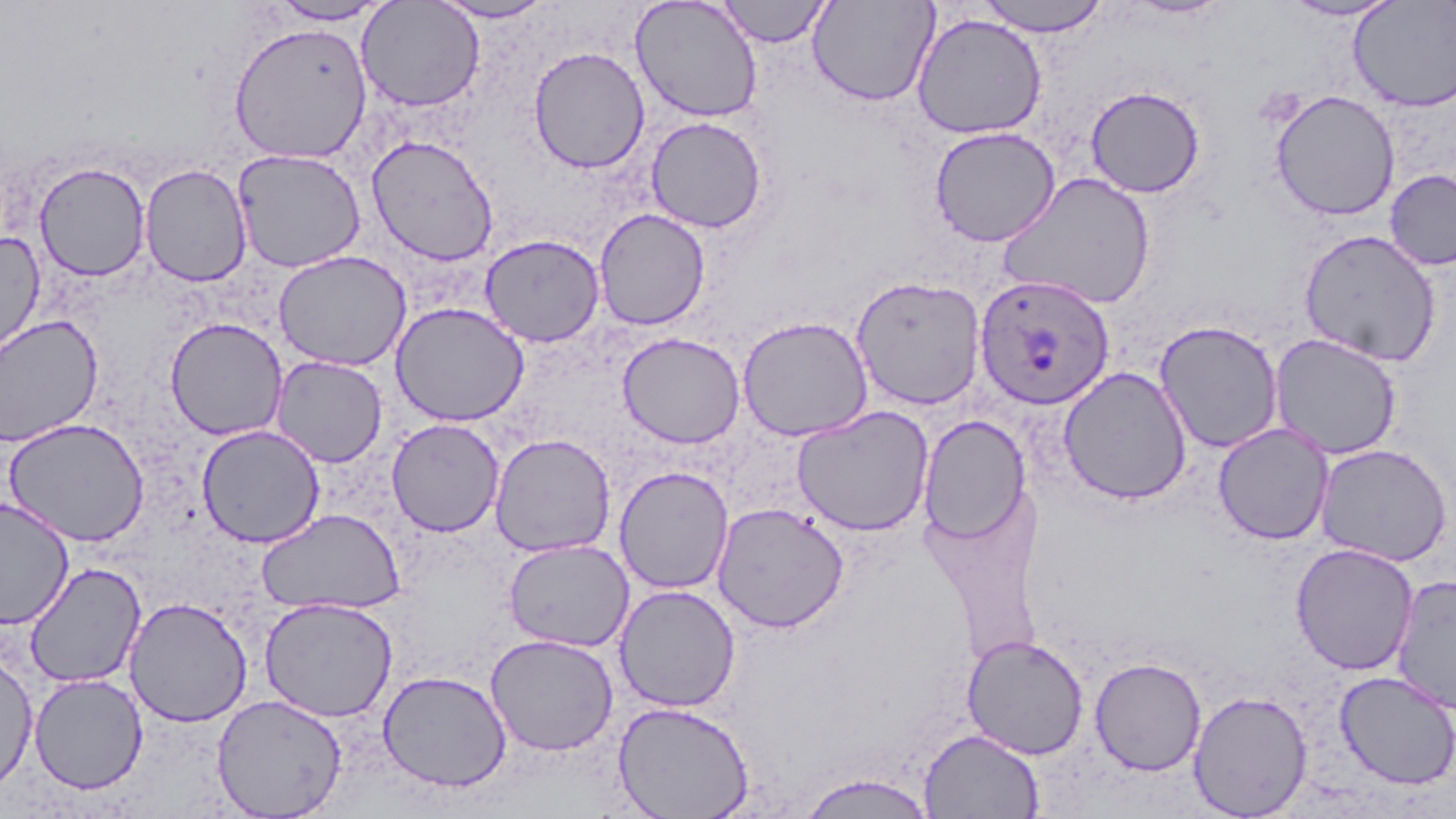 Approximate bounding boxes as (x1, y1, x2, y2) in pixels. Plasmodium ovale-infected red blood cell locations: (973, 275, 1114, 410). Uninfected red blood cell locations: (428, 0, 557, 23), (630, 0, 763, 123), (717, 0, 833, 47), (807, 0, 940, 107), (974, 0, 1111, 36), (1120, 0, 1234, 20), (1280, 0, 1403, 22), (269, 1, 392, 26), (356, 1, 485, 112), (1349, 1, 1456, 113), (911, 13, 1047, 139), (228, 21, 374, 164), (528, 46, 650, 174), (1084, 85, 1206, 198), (1270, 89, 1401, 221), (646, 116, 768, 233), (929, 126, 1060, 246), (366, 134, 499, 266), (232, 149, 366, 273), (34, 160, 150, 281), (139, 163, 253, 287), (1385, 168, 1456, 271), (997, 171, 1156, 310), (593, 208, 710, 331), (1298, 228, 1442, 366), (0, 231, 46, 363), (479, 234, 606, 347), (273, 250, 411, 371), (851, 275, 986, 411), (391, 302, 529, 427), (0, 314, 104, 447), (736, 315, 873, 441), (165, 317, 288, 441), (1154, 320, 1284, 454), (618, 332, 745, 449), (1269, 332, 1403, 460), (271, 356, 388, 468), (1057, 366, 1193, 505), (791, 405, 934, 537), (918, 416, 1031, 543), (3, 418, 151, 547), (386, 418, 505, 537), (1213, 423, 1333, 544), (196, 424, 326, 548), (489, 433, 616, 558), (1314, 443, 1453, 566), (614, 466, 734, 595), (0, 497, 75, 630), (712, 502, 850, 633), (255, 508, 406, 615), (503, 539, 634, 652), (1291, 543, 1419, 675), (24, 562, 146, 689), (1391, 574, 1456, 715), (614, 584, 741, 713), (123, 596, 253, 727), (260, 596, 399, 723), (485, 633, 619, 756), (961, 634, 1089, 759), (0, 651, 38, 795), (1089, 657, 1207, 776), (377, 670, 512, 793), (1333, 671, 1456, 790), (28, 673, 148, 794), (1188, 690, 1313, 819), (212, 694, 348, 818), (613, 701, 755, 819), (919, 728, 1045, 817), (796, 772, 937, 818). Slide-level diagnosis: Plasmodium ovale. Image is 1456×819 pixels. One field of a larger specimen. Optical microscopy. Captured at 1000x magnification. Thin blood film. May-Grünwald-Giemsa-stained preparation.